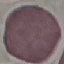
result = no malaria parasites detected
image type = cell patch, automatically extracted from a larger field of view and resized to 64 × 64 pixels
stain = Giemsa
capture = smartphone camera at the microscope eyepiece
preparation = thin smear